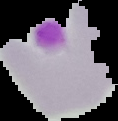
Summary:
  - Image type: segmented cell region on a black background
  - Preparation: thin blood film
  - Image size: 118×121 pixels
  - Result: no malaria parasites seen